State which parasite is depicted.
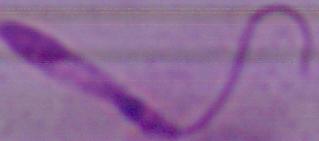

Leishmania.

magnification: 1000x
modality: photomicrograph